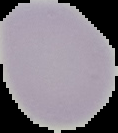

{
  "image_type": "cell region segmented out of the field of view; surrounding area masked to black",
  "preparation": "thin blood film",
  "result": "no Plasmodium parasites detected",
  "image_size": "118×133 pixels"
}